Comment on the morphology of the erythrocytes.
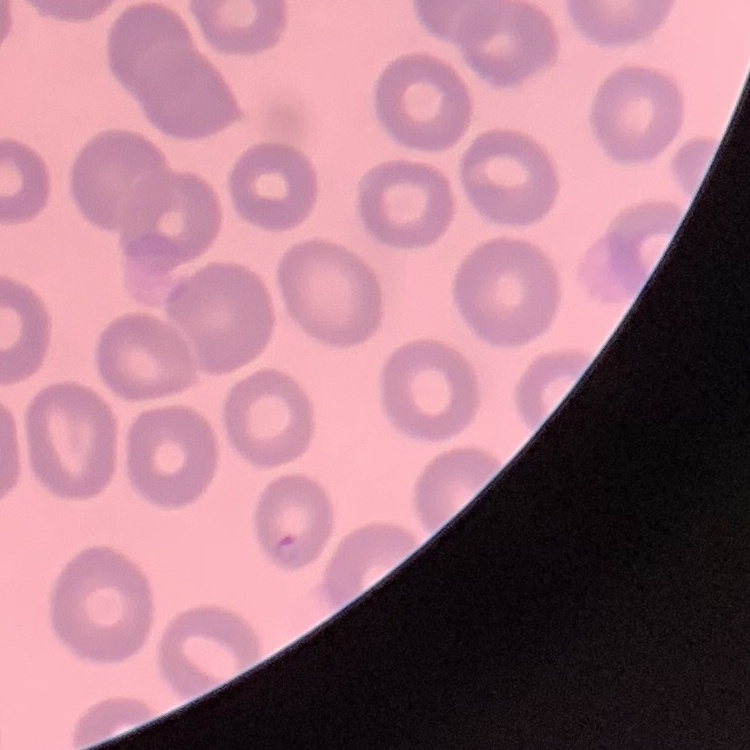
They show no rouleaux formation.

Summary:
  - Image type: square crop of a larger photomicrograph
  - Stain: Field's or Giemsa
  - Preparation: thin blood film